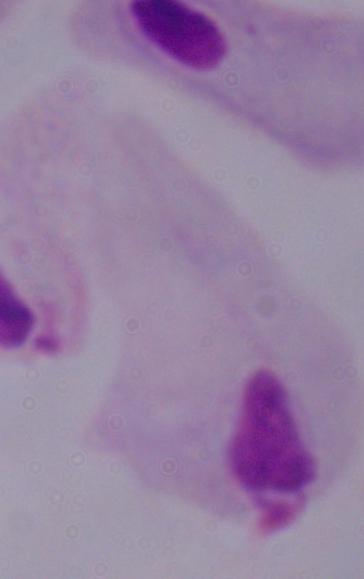

Summary:
  - Modality: photomicrograph
  - Identification: trichomonad
  - Magnification: 1000x